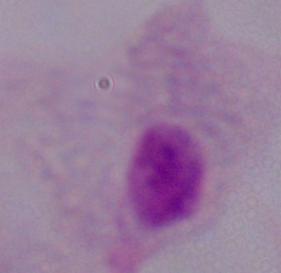

{
  "modality": "photomicrograph",
  "magnification": "1000x",
  "identification": "trichomonad"
}